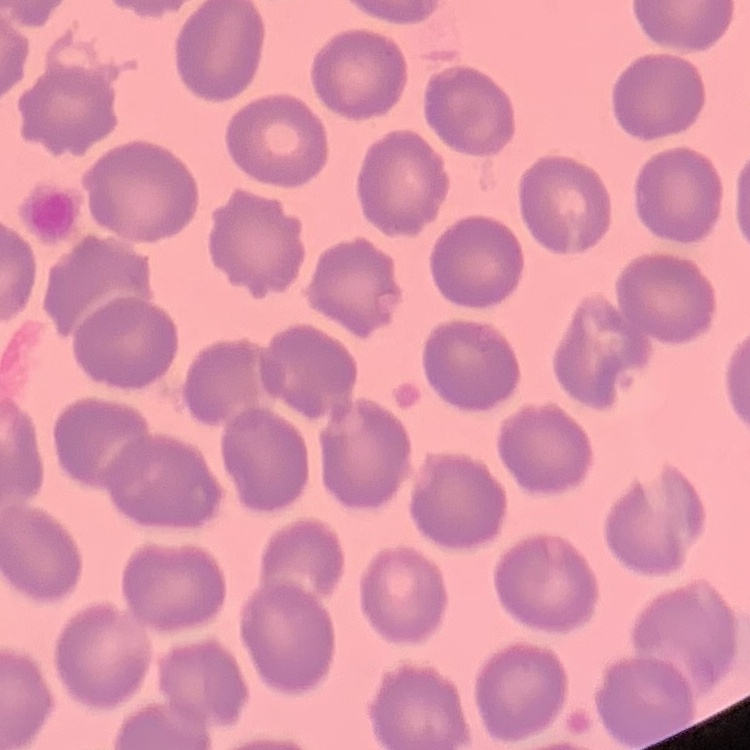
The erythrocytes exhibit no rouleaux formation. Thin blood film. One tile cut from a larger photomicrograph. Field's or Giemsa stain.